Classify this cell by malaria status.
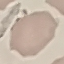
Uninfected.

Summary:
  - Stain: Giemsa
  - Image type: automatically extracted cell patch, resized to 64 × 64 pixels
  - Capture: smartphone camera at the microscope eyepiece
  - Preparation: thin blood smear